Assess the morphology of the red blood cells.
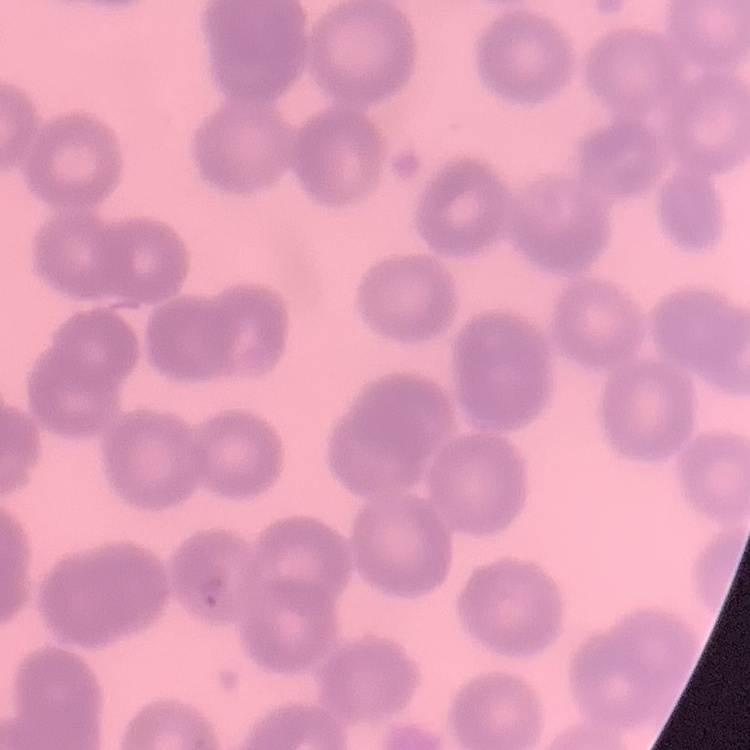

No rouleaux formation.

preparation: thin peripheral smear
image_type: square crop of a larger photomicrograph
stain: Field's or Giemsa